Assess this cell for malaria.
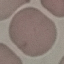
Uninfected.

Giemsa-stained preparation. Thin smear of blood. Photographed with a smartphone camera at the microscope eyepiece. Cell patch, automatically extracted from a larger field of view and resized to 64 × 64 pixels.